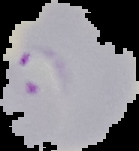

Summary:
  - Preparation: thin blood smear
  - Result: malaria parasites detected
  - Image size: 139×151 pixels
  - Image type: cell region segmented out of the field of view; surrounding area masked to black